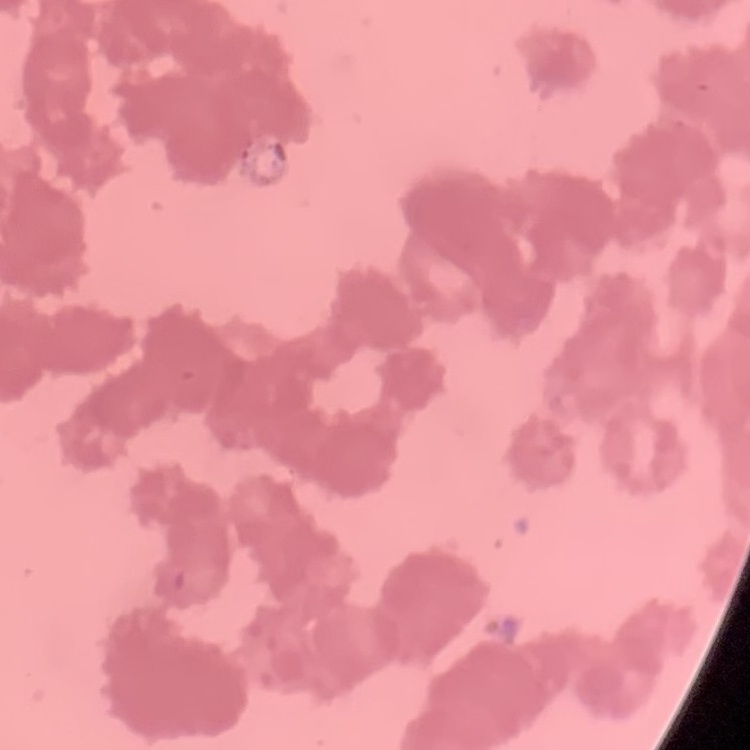
red_blood_cell_morphology: rouleaux formation
preparation: thin peripheral smear
image_type: square crop of a larger photomicrograph
stain: Field's or Giemsa